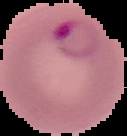

Summary:
  - Image type: segmented cell region on a black background
  - Image size: 127×136 pixels
  - Result: malaria parasites identified
  - Preparation: thin blood film